Describe the morphology of the red blood cells.
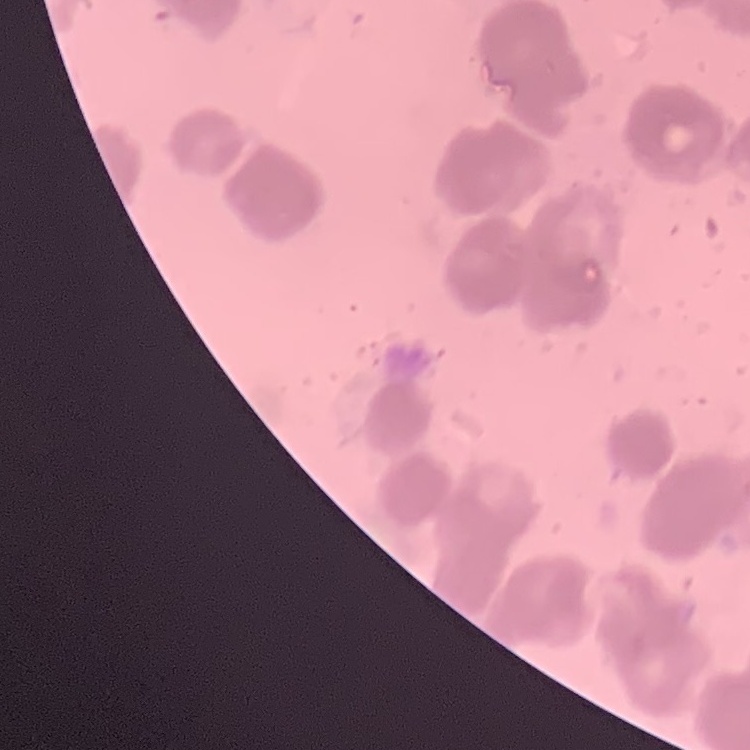
Rouleaux formation.

Summary:
  - Image type: square crop of a larger photomicrograph
  - Stain: Field's or Giemsa
  - Preparation: thin blood smear